Point out each Plasmodium parasite and each leukocyte.
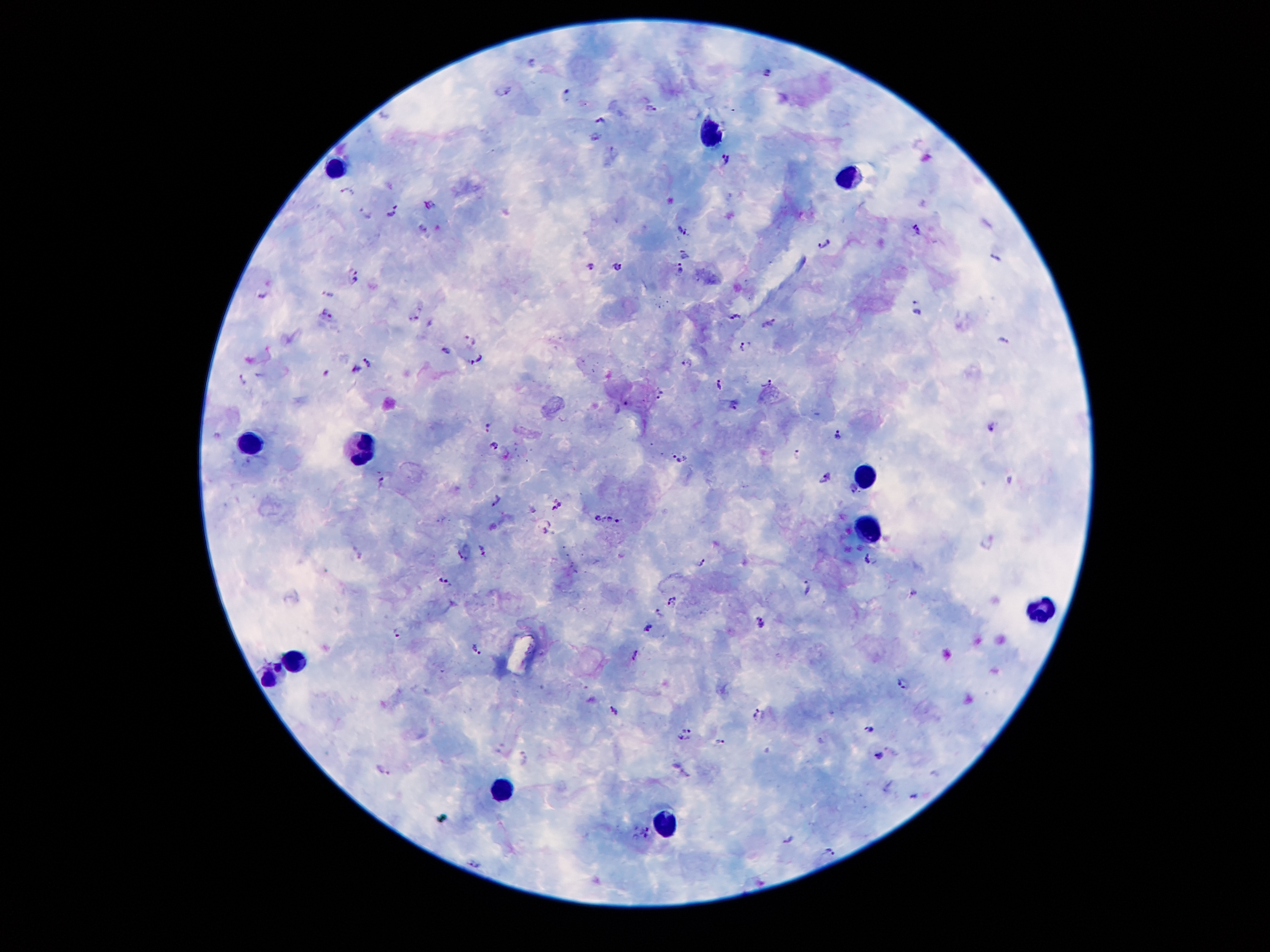
Approximate centers as {x, y} in pixels.
Plasmodium parasites: {533, 62}, {766, 73}, {502, 91}, {566, 94}, {652, 106}, {600, 121}, {594, 138}, {614, 152}, {726, 157}, {348, 190}, {429, 203}, {391, 210}, {370, 212}, {421, 224}, {917, 227}, {681, 232}, {824, 245}, {686, 253}, {996, 258}, {589, 264}, {617, 264}, {679, 271}, {355, 276}, {263, 293}, {329, 293}, {918, 307}, {327, 313}, {735, 315}, {414, 319}, {770, 320}, {470, 338}, {1004, 340}, {744, 345}, {447, 349}, {476, 359}, {367, 360}, {686, 361}, {354, 370}, {327, 373}, {242, 380}, {719, 383}, {768, 384}, {660, 393}, {732, 403}, {487, 424}, {992, 425}, {838, 435}, {495, 444}, {797, 454}, {680, 459}, {825, 476}, {383, 480}, {497, 498}, {556, 503}, {596, 515}, {607, 518}, {618, 521}, {546, 530}, {484, 548}, {461, 556}, {868, 558}, {704, 563}, {446, 580}, {807, 585}, {914, 593}, {673, 600}, {659, 614}, {761, 623}, {648, 627}, {398, 632}, {476, 648}, {636, 655}, {904, 683}, {614, 709}, {758, 714}, {687, 725}, {871, 728}, {683, 738}, {722, 742}, {879, 755}, {524, 760}, {385, 771}, {914, 795}, {648, 832}, {789, 840}, {831, 850}, {475, 864}.
Leukocytes: {709, 129}, {337, 162}, {849, 172}, {249, 442}, {360, 448}, {867, 477}, {868, 522}, {1042, 609}, {295, 661}, {274, 677}, {499, 790}, {663, 814}.

preparation = thick peripheral-blood smear
stain = Giemsa
patient malaria status = positive for Plasmodium falciparum
image size = 1270×952 pixels
field of view = one from this slide
magnification = 100x
capture = smartphone through the microscope eyepiece